Mark where platelets are.
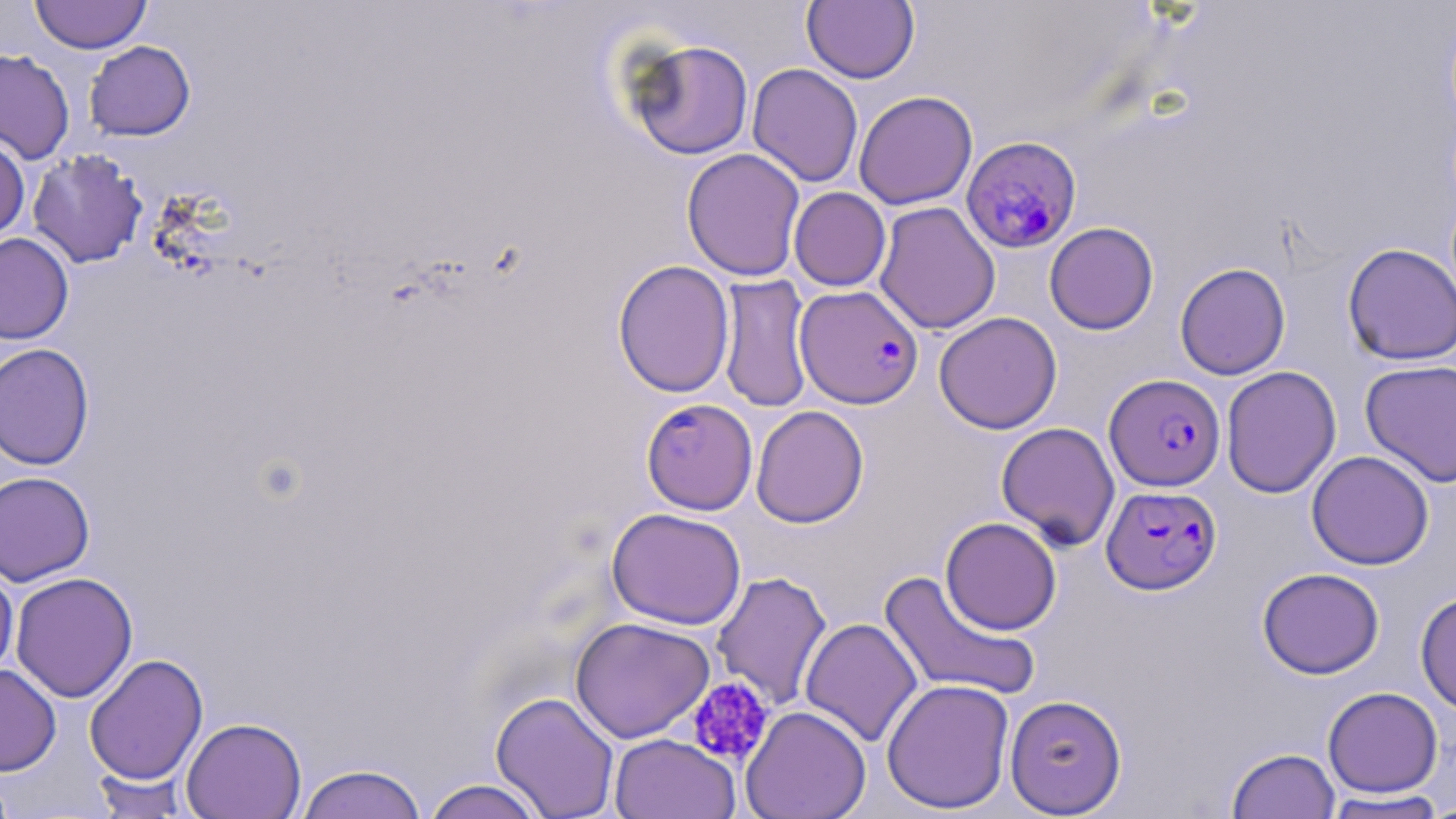

Approximate bounding boxes as (x1, y1, x2, y2) in pixels.
Platelets: (686, 676, 776, 768).

Summary:
  - Uninfected red blood cell locations: (30, 0, 152, 54), (802, 0, 919, 83), (624, 38, 755, 160), (84, 40, 195, 141), (0, 49, 75, 164), (747, 63, 864, 187), (853, 90, 978, 210), (0, 135, 30, 243), (681, 148, 805, 281), (27, 149, 148, 269), (789, 187, 891, 291), (874, 201, 1000, 334), (1044, 221, 1159, 335), (0, 232, 74, 344), (1341, 243, 1456, 365), (612, 260, 735, 398), (1174, 262, 1291, 380), (717, 275, 813, 413), (934, 311, 1062, 434), (0, 342, 96, 470), (1360, 358, 1456, 488), (1221, 365, 1342, 499), (751, 405, 869, 528), (996, 421, 1121, 550), (1306, 450, 1434, 570), (0, 471, 95, 586), (607, 507, 747, 630), (940, 516, 1061, 634), (0, 561, 19, 684), (1257, 567, 1384, 679), (878, 570, 1041, 702), (10, 571, 138, 703), (711, 571, 832, 710), (1415, 590, 1456, 715), (570, 616, 715, 743), (799, 617, 923, 748), (84, 653, 208, 785), (0, 663, 61, 776), (881, 678, 1015, 814), (1322, 686, 1443, 797), (491, 691, 620, 818), (1005, 694, 1127, 816), (741, 706, 871, 818), (181, 716, 307, 818), (609, 733, 740, 819), (1226, 747, 1340, 819), (295, 763, 428, 819), (0, 769, 18, 819), (90, 770, 193, 817), (420, 778, 548, 819), (1322, 791, 1447, 818)
  - Plasmodium falciparum-infected red blood cell locations: (960, 135, 1082, 255), (795, 285, 924, 408), (1104, 373, 1225, 491), (641, 399, 757, 515), (1101, 485, 1222, 595)
  - Slide-level diagnosis: Plasmodium falciparum
  - Modality: light microscopy
  - Preparation: thin blood film
  - Magnification: 1000x
  - Image size: 1456×819 pixels
  - Field of view: single
  - Stain: May-Grünwald-Giemsa